Name the blood parasite species.
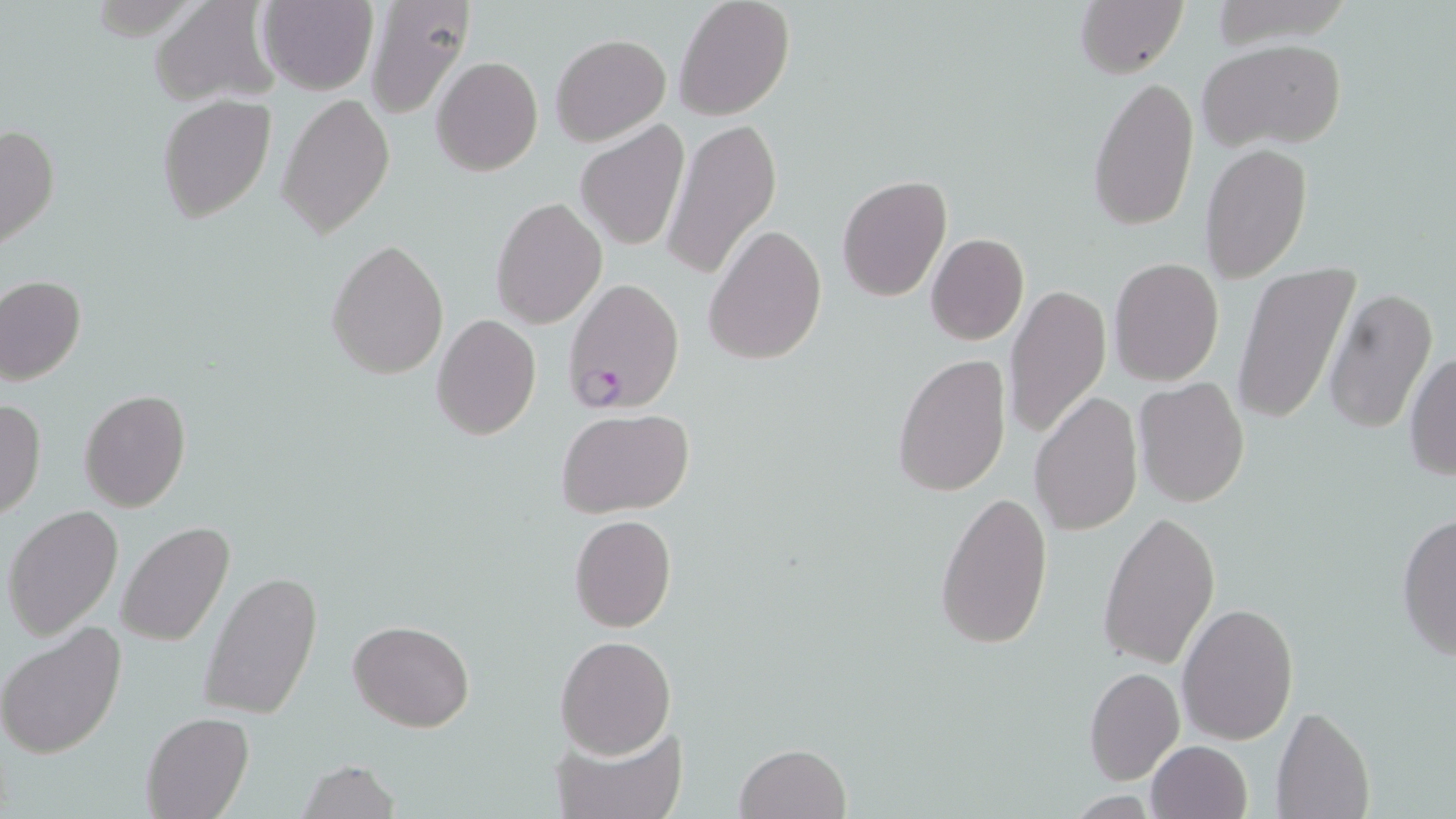

Plasmodium falciparum.

uninfected red blood cell locations = approximate bounding boxes as named x1/y1/x2/y2 corners in pixels: (x1=150, y1=0, x2=284, y2=108), (x1=258, y1=0, x2=378, y2=96), (x1=361, y1=0, x2=476, y2=120), (x1=673, y1=0, x2=796, y2=120), (x1=1075, y1=0, x2=1188, y2=79), (x1=551, y1=32, x2=671, y2=146), (x1=1199, y1=39, x2=1347, y2=152), (x1=431, y1=56, x2=542, y2=176), (x1=1086, y1=74, x2=1200, y2=232), (x1=277, y1=93, x2=395, y2=237), (x1=156, y1=94, x2=276, y2=222), (x1=662, y1=116, x2=781, y2=285), (x1=575, y1=120, x2=690, y2=252), (x1=0, y1=124, x2=61, y2=252), (x1=1200, y1=143, x2=1313, y2=283), (x1=836, y1=175, x2=954, y2=303), (x1=491, y1=197, x2=608, y2=328), (x1=704, y1=224, x2=827, y2=368), (x1=925, y1=232, x2=1029, y2=346), (x1=326, y1=238, x2=449, y2=381), (x1=1109, y1=257, x2=1224, y2=388), (x1=1232, y1=263, x2=1360, y2=428), (x1=1, y1=275, x2=86, y2=385), (x1=1004, y1=284, x2=1112, y2=440), (x1=1322, y1=287, x2=1436, y2=435), (x1=432, y1=314, x2=541, y2=440), (x1=1405, y1=352, x2=1456, y2=481), (x1=892, y1=353, x2=1012, y2=497), (x1=1135, y1=376, x2=1251, y2=508), (x1=79, y1=389, x2=191, y2=512), (x1=1029, y1=392, x2=1142, y2=535), (x1=0, y1=399, x2=46, y2=520), (x1=557, y1=408, x2=697, y2=516), (x1=935, y1=488, x2=1053, y2=651), (x1=3, y1=505, x2=124, y2=639), (x1=1099, y1=509, x2=1218, y2=668), (x1=1395, y1=512, x2=1456, y2=662), (x1=569, y1=513, x2=676, y2=632), (x1=118, y1=521, x2=235, y2=647), (x1=198, y1=568, x2=324, y2=721), (x1=1176, y1=600, x2=1298, y2=744), (x1=347, y1=619, x2=475, y2=733), (x1=0, y1=623, x2=127, y2=759), (x1=554, y1=635, x2=675, y2=759), (x1=1084, y1=665, x2=1183, y2=784), (x1=1270, y1=703, x2=1374, y2=819), (x1=140, y1=712, x2=253, y2=819), (x1=552, y1=721, x2=687, y2=819), (x1=1145, y1=740, x2=1252, y2=819), (x1=735, y1=743, x2=851, y2=818), (x1=299, y1=759, x2=400, y2=819)
image size = 1456×819 pixels
modality = optical microscopy
stain = May-Grünwald-Giemsa
magnification = 1000x
field of view = one of a larger specimen
Plasmodium falciparum-infected red blood cell locations = approximate bounding boxes as named x1/y1/x2/y2 corners in pixels: (x1=564, y1=278, x2=684, y2=414)
preparation = thin blood smear